State the blood parasite species.
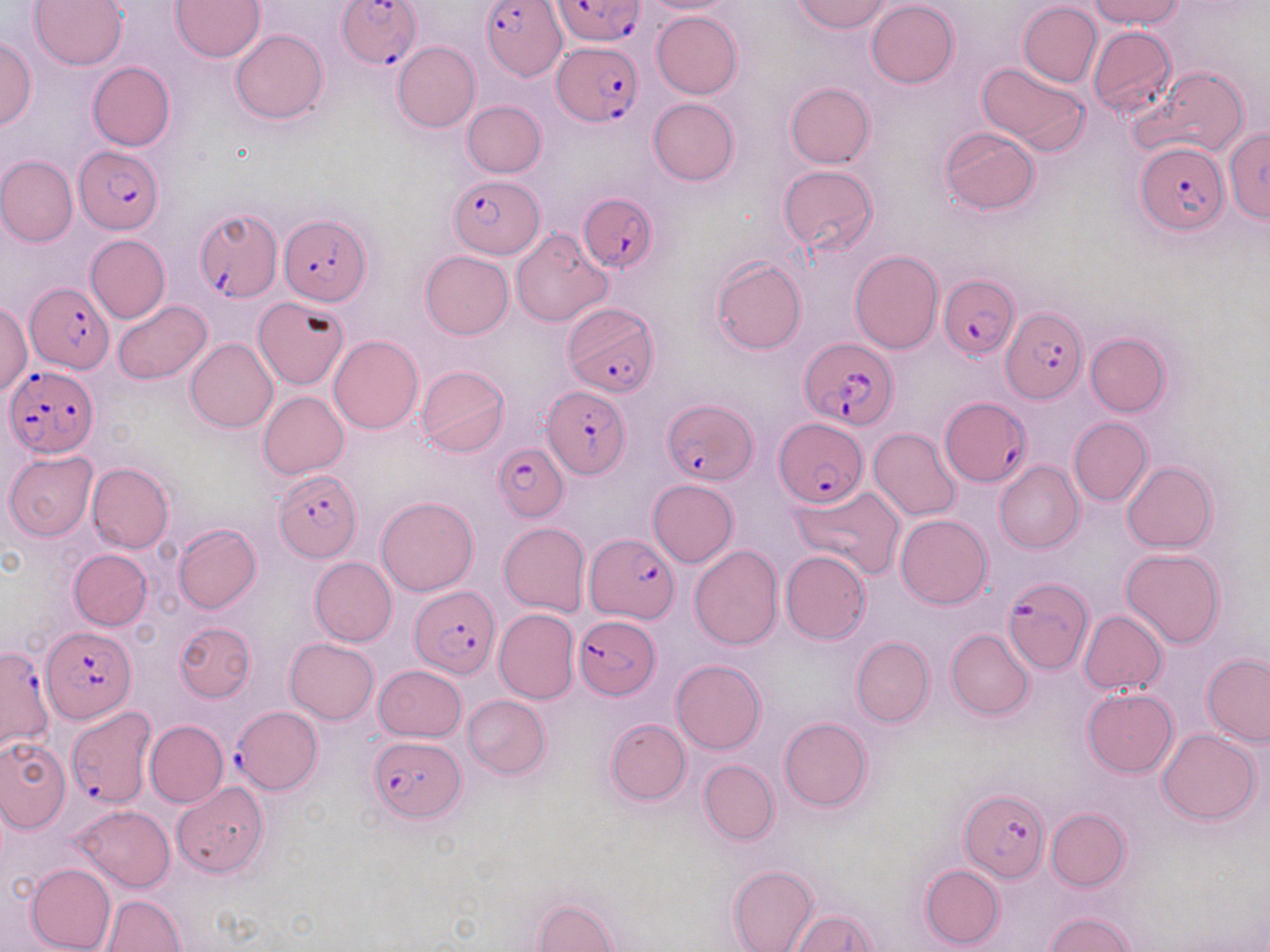
Plasmodium falciparum.

Approximate bounding boxes as [x1, y1, x2, y2] in pixels. Uninfected red blood cell locations: [28, 0, 128, 71], [172, 0, 265, 61], [791, 0, 893, 34], [1089, 0, 1184, 28], [637, 1, 741, 14], [865, 1, 959, 88], [1018, 2, 1101, 87], [652, 11, 742, 98], [1088, 25, 1177, 118], [230, 28, 328, 124], [0, 36, 36, 129], [392, 41, 479, 132], [977, 61, 1090, 155], [88, 62, 175, 151], [1136, 67, 1249, 158], [785, 81, 875, 167], [647, 97, 740, 186], [463, 101, 546, 178], [940, 126, 1040, 215], [1224, 128, 1270, 223], [0, 155, 78, 246], [778, 165, 877, 255], [510, 228, 612, 326], [86, 235, 171, 323], [850, 250, 942, 354], [420, 251, 513, 339], [711, 257, 806, 354], [255, 297, 348, 390], [112, 300, 213, 385], [1, 302, 32, 395], [1084, 333, 1172, 417], [328, 335, 424, 435], [185, 338, 279, 434], [416, 365, 510, 457], [258, 391, 350, 479], [1068, 417, 1152, 506], [869, 427, 962, 521], [4, 450, 98, 541], [993, 460, 1084, 554], [1122, 461, 1218, 552], [87, 462, 174, 553], [648, 479, 738, 567], [791, 483, 904, 581], [376, 496, 479, 596], [895, 514, 993, 609], [499, 522, 590, 616], [172, 523, 261, 613], [690, 546, 783, 649], [69, 549, 153, 630], [1120, 549, 1225, 649], [780, 551, 871, 644], [309, 556, 397, 645], [494, 609, 579, 703], [1080, 610, 1167, 695], [174, 621, 255, 702], [946, 628, 1034, 720], [851, 635, 934, 726], [285, 637, 379, 724], [1202, 654, 1270, 746], [671, 660, 766, 754], [374, 664, 466, 742], [1083, 688, 1179, 776], [462, 694, 550, 780], [779, 716, 872, 813], [605, 719, 692, 805], [145, 720, 228, 809], [1158, 728, 1261, 825], [0, 737, 69, 833], [699, 759, 779, 845], [172, 782, 270, 878], [72, 805, 174, 892], [1045, 808, 1131, 891], [25, 863, 115, 952], [919, 863, 1004, 949], [728, 864, 818, 952], [101, 894, 185, 952], [532, 897, 617, 951], [791, 910, 878, 951], [1044, 912, 1135, 952]. Plasmodium falciparum-infected red blood cell locations: [337, 0, 421, 67], [553, 0, 643, 46], [482, 1, 565, 79], [553, 43, 644, 124], [1135, 141, 1228, 234], [74, 147, 163, 233], [450, 175, 544, 258], [580, 191, 659, 275], [193, 205, 281, 304], [277, 215, 370, 307], [939, 274, 1019, 359], [25, 284, 113, 374], [563, 302, 660, 397], [1002, 308, 1087, 403], [800, 339, 897, 430], [4, 365, 97, 458], [541, 384, 630, 477], [941, 396, 1031, 488], [663, 400, 757, 486], [775, 419, 868, 506], [492, 445, 569, 520], [273, 470, 363, 563], [584, 535, 679, 622], [1002, 576, 1094, 676], [412, 584, 499, 676], [573, 613, 661, 699], [41, 626, 135, 723], [0, 646, 55, 754], [233, 705, 324, 796], [66, 707, 156, 809], [369, 736, 466, 822], [962, 789, 1047, 882]. May-Grünwald-Giemsa-stained preparation. Captured at 1000x magnification. Thin blood smear. One field of a larger specimen. Image is 1270×952 pixels. Light microscopy.